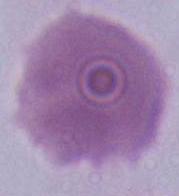

Summary:
  - Magnification: 1000x
  - Identification: red blood cell
  - Modality: micrograph